Report the malaria status of this cell.
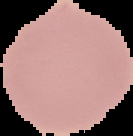

Uninfected.

Image is 133×136 pixels. From a thin blood smear. Cell region segmented out of the field of view; the surrounding area is masked to black.